Assess this cell for malaria.
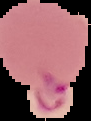

Parasitized.

{
  "image_size": "91×121 pixels",
  "preparation": "thin blood smear",
  "image_type": "segmented cell region on a black background"
}